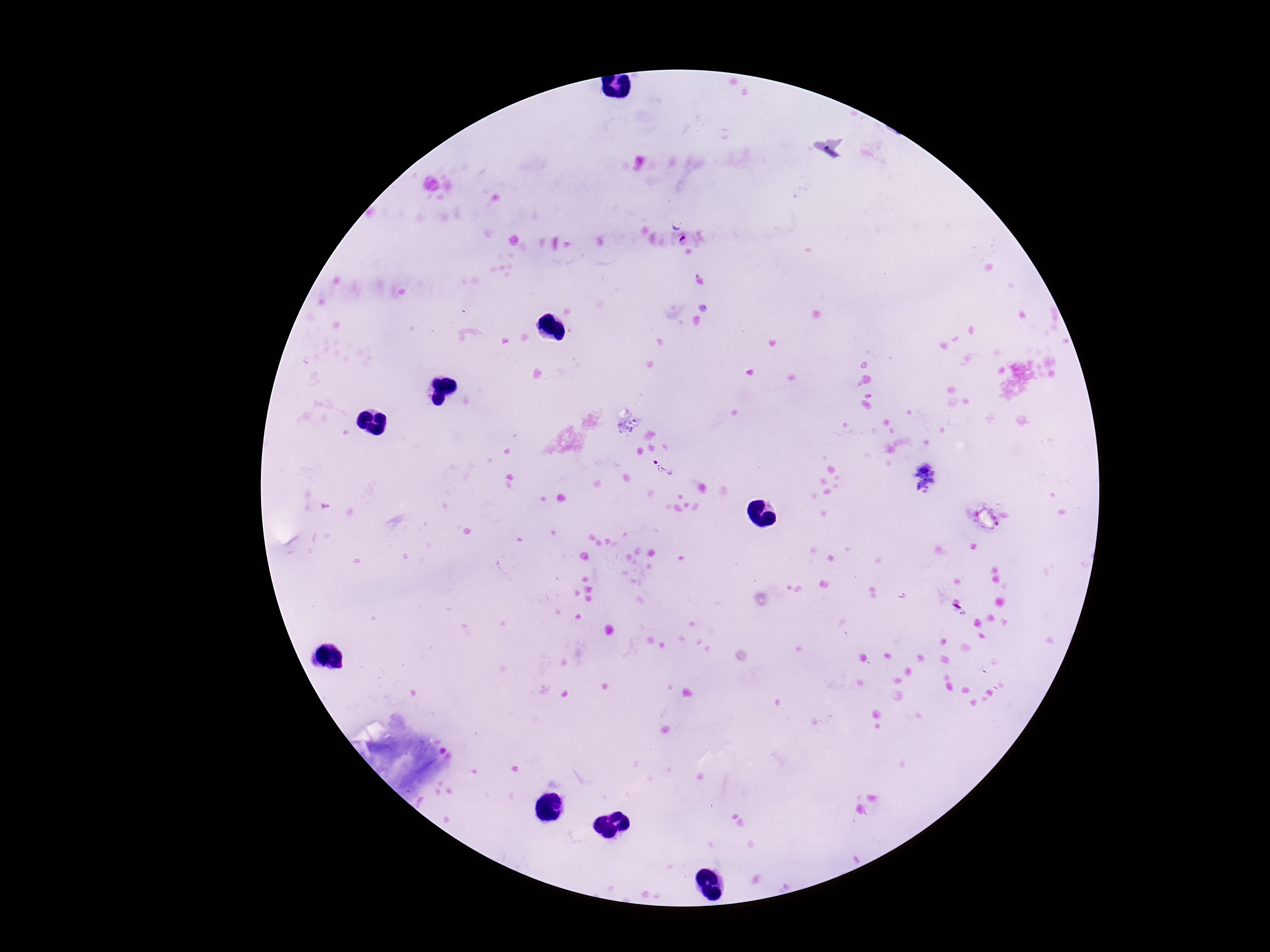 Approximate object centers, in pixels from the top-left corner. Plasmodium parasite locations: (x=662, y=467). Thick blood smear. Giemsa stain. 100x magnification. Smartphone photograph taken through the microscope eyepiece. Single field of view. Image is 1270×952 pixels. Patient malaria status: infected.